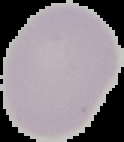

image size = 124×142 pixels
preparation = thin blood film
result = no Plasmodium parasites detected
image type = segmented cell region with the area outside set to black